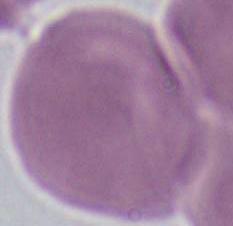

{
  "identification": "erythrocyte",
  "modality": "micrograph",
  "magnification": "1000x"
}